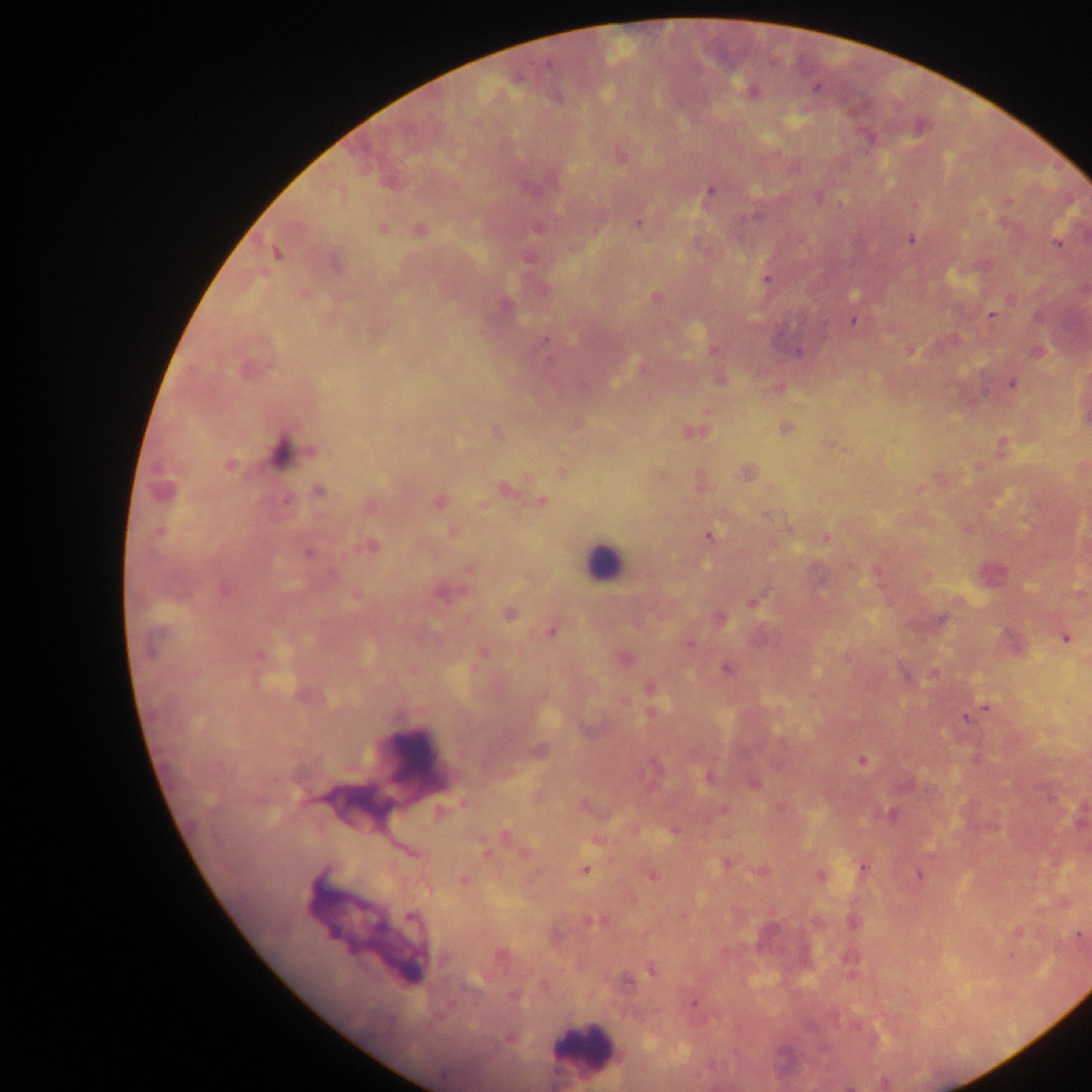

Approximate centers as [x, y] in pixels.
Summary:
  - Leukocyte locations: [602, 563], [409, 758], [357, 806], [376, 927], [586, 1047]
  - Plasmodium parasite locations: [815, 87], [752, 92], [621, 155], [709, 191], [1007, 200], [915, 205], [756, 214], [637, 222], [1004, 223], [538, 227], [381, 228], [419, 229], [910, 238], [1057, 243], [275, 252], [529, 256], [335, 262], [766, 278], [303, 293], [854, 294], [655, 296], [1011, 299], [505, 304], [992, 314], [854, 320], [953, 338], [545, 339], [713, 351], [910, 351], [1037, 351], [798, 352], [641, 366], [720, 378], [1012, 384], [776, 388], [576, 424], [785, 428], [692, 432], [498, 434], [896, 439], [829, 444], [1002, 445], [283, 452], [229, 465], [560, 471], [747, 472], [662, 474], [939, 477], [700, 481], [504, 487], [921, 488], [162, 490], [318, 490], [286, 500], [438, 502], [540, 502], [369, 505], [482, 505], [766, 514], [967, 528], [453, 531], [159, 532], [708, 535], [825, 538], [371, 546], [307, 552], [469, 567], [877, 570], [990, 573], [926, 575], [528, 577], [445, 592], [355, 596], [753, 601], [509, 613], [718, 618], [940, 620], [552, 630], [1065, 637], [1011, 641], [688, 643], [482, 651], [259, 657], [625, 657], [725, 668], [933, 673], [651, 688], [651, 704], [985, 707], [965, 717], [538, 751], [862, 760], [653, 769], [709, 777], [753, 783], [462, 803], [582, 805], [722, 809], [1080, 814], [889, 815], [674, 831], [505, 836], [596, 839], [485, 850], [726, 862], [862, 868], [583, 870], [761, 870], [651, 875], [820, 875], [918, 875], [463, 880], [1065, 903], [592, 920], [853, 923], [1017, 932], [1079, 936], [501, 956], [651, 968], [627, 980], [693, 1003], [509, 1038]
  - Image size: 1092×1092 pixels
  - Country: Ghana
  - Field of view: single
  - Capture: mobile-phone photograph through a microscope
  - Preparation: thick blood film